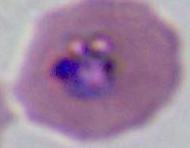
A Plasmodium parasite is shown. 400x or 1000x magnification. Photomicrograph.